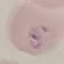
malaria status = parasitized
image type = cell patch, automatically extracted from a larger field of view and resized to 64 × 64 pixels
stain = Giemsa
preparation = thin blood film
capture = smartphone through the microscope eyepiece